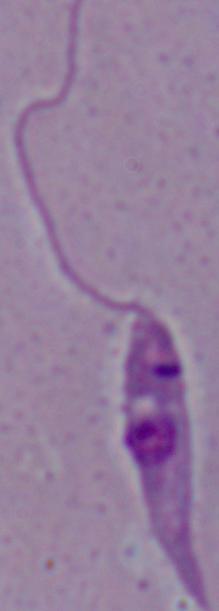 A Leishmania parasite is shown. 1000x magnification. Micrograph.